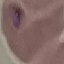
{
  "malaria_status": "parasitized",
  "preparation": "thin blood smear",
  "image_type": "automatically extracted cell patch, resized to 64 × 64 pixels",
  "capture": "smartphone through the microscope eyepiece",
  "stain": "Giemsa"
}